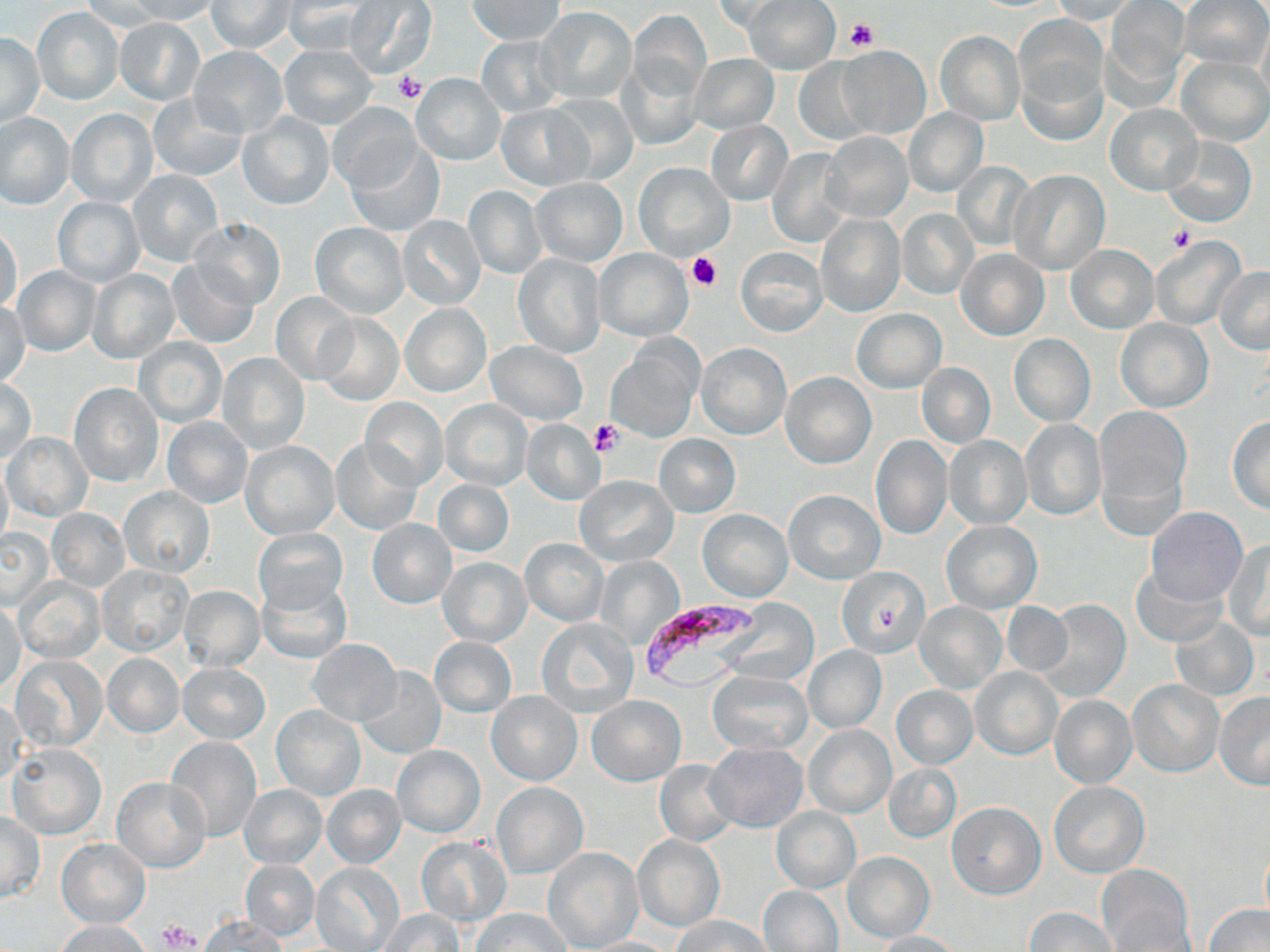

Approximate bounding boxes as (x1,y1)-(x2,y2) corner pairs in pixels. Platelet locations: (844,18)-(878,53), (392,72)-(428,105), (1166,228)-(1193,252), (686,252)-(722,292), (591,420)-(622,456), (158,920)-(201,950). Plasmodium falciparum-infected red blood cell locations: (643,604)-(760,690). Uninfected red blood cell locations: (122,0)-(222,24), (468,0)-(564,44), (709,0)-(793,32), (742,0)-(840,75), (1051,0)-(1136,23), (1180,0)-(1268,69), (80,1)-(167,34), (207,1)-(294,53), (281,1)-(373,55), (344,1)-(436,78), (1104,2)-(1190,97), (32,7)-(125,106), (536,7)-(636,104), (627,10)-(711,99), (1016,16)-(1105,121), (116,18)-(205,104), (1257,19)-(1270,109), (934,30)-(1024,126), (1,33)-(44,128), (476,35)-(564,118), (487,37)-(573,190), (280,43)-(377,129), (189,47)-(287,137), (835,47)-(930,139), (616,52)-(707,152), (689,54)-(778,135), (1177,55)-(1270,147), (793,57)-(876,145), (411,73)-(505,165), (148,91)-(246,182), (548,93)-(638,185), (328,102)-(421,193), (1107,103)-(1201,194), (497,104)-(590,191), (903,108)-(988,197), (67,109)-(158,207), (0,112)-(75,209), (236,114)-(335,210), (706,120)-(792,204), (821,132)-(912,223), (1161,135)-(1256,228), (346,143)-(443,236), (767,148)-(851,245), (635,161)-(734,260), (953,162)-(1035,250), (129,169)-(224,267), (1009,169)-(1109,275), (530,178)-(628,265), (462,184)-(547,280), (53,197)-(144,286), (403,200)-(539,292), (898,209)-(977,298), (815,213)-(905,317), (396,214)-(488,311), (190,217)-(286,311), (0,223)-(23,314), (309,223)-(410,319), (1151,239)-(1245,330), (1066,244)-(1159,334), (735,246)-(827,335), (956,247)-(1050,342), (594,248)-(693,341), (513,254)-(607,357), (165,259)-(259,348), (12,265)-(101,357), (1215,266)-(1270,353), (86,269)-(179,363), (270,291)-(360,385), (0,300)-(31,385), (400,303)-(491,398), (853,308)-(946,393), (315,313)-(404,406), (1116,318)-(1214,411), (1008,334)-(1096,427), (134,337)-(228,428), (486,341)-(588,425), (607,342)-(702,442), (696,342)-(792,440), (218,351)-(309,453), (917,363)-(995,448), (781,372)-(877,468), (1,377)-(37,464), (69,382)-(163,486), (359,398)-(449,490), (439,399)-(533,491), (1095,406)-(1191,508), (1226,416)-(1270,513), (162,417)-(252,508), (520,419)-(605,505), (1020,419)-(1108,521), (3,433)-(92,520), (653,433)-(741,517), (870,435)-(954,541), (944,435)-(1032,530), (331,439)-(421,535), (241,440)-(340,539), (0,456)-(13,553), (574,475)-(678,566), (433,479)-(514,557), (120,487)-(214,576), (783,490)-(884,583), (1146,507)-(1248,607), (47,509)-(130,592), (698,509)-(792,602), (366,517)-(457,609), (940,520)-(1041,612), (0,527)-(54,610), (254,527)-(348,614), (520,538)-(609,626), (1223,539)-(1270,641), (437,556)-(532,646), (595,558)-(684,647), (98,564)-(194,657), (1130,564)-(1225,646), (837,569)-(927,666), (15,577)-(106,663), (258,578)-(353,664), (177,585)-(265,673), (1038,599)-(1131,702), (0,601)-(25,695), (913,601)-(1007,694), (723,602)-(820,686), (1002,602)-(1073,675), (537,618)-(639,716), (1170,618)-(1260,701), (429,636)-(517,716), (307,638)-(402,725), (803,645)-(886,733), (103,653)-(183,736), (12,655)-(106,751), (178,662)-(270,744), (358,666)-(446,759), (970,667)-(1062,760), (709,671)-(812,755), (1127,679)-(1223,776), (891,685)-(978,768), (486,690)-(581,786), (1214,693)-(1270,789), (587,694)-(686,786), (1049,694)-(1136,788), (0,695)-(26,788), (272,705)-(366,801), (804,725)-(895,817), (166,737)-(262,840), (704,742)-(808,833), (8,745)-(106,839), (392,745)-(486,837), (655,758)-(740,848), (884,763)-(961,842), (113,776)-(211,871), (491,780)-(589,880), (1049,781)-(1148,877), (322,784)-(406,868), (238,785)-(327,867), (947,801)-(1045,899), (771,806)-(860,893), (0,812)-(44,902), (632,834)-(724,932), (416,837)-(511,926), (56,838)-(151,927), (1260,844)-(1270,924), (543,847)-(644,951), (842,850)-(935,943), (240,860)-(320,939), (311,863)-(405,952), (1096,864)-(1193,950), (758,885)-(843,951), (1203,904)-(1270,952), (1026,907)-(1117,952), (473,908)-(570,952), (378,909)-(464,952), (199,915)-(288,951), (671,915)-(773,952), (55,920)-(153,952), (869,929)-(966,951), (577,936)-(680,951). Slide-level diagnosis: Plasmodium falciparum. May-Grünwald-Giemsa stain. Light microscopy. Image is 1270×952 pixels. Thin blood film. One field of a larger specimen. Captured at 1000x magnification.